State which parasite is depicted.
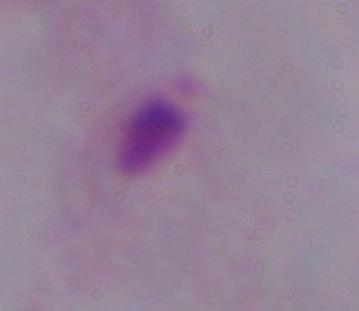
A trichomonad.

Summary:
  - Magnification: 1000x
  - Modality: micrograph